Report the malaria status of this cell.
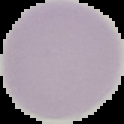

It is uninfected.

image size = 124×124 pixels
image type = cell region segmented out of the field of view; surrounding area masked to black
preparation = thin blood film